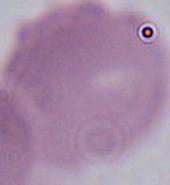

identification = red blood cell
magnification = 1000x
modality = photomicrograph